Locate every blood parasite and identify its species.
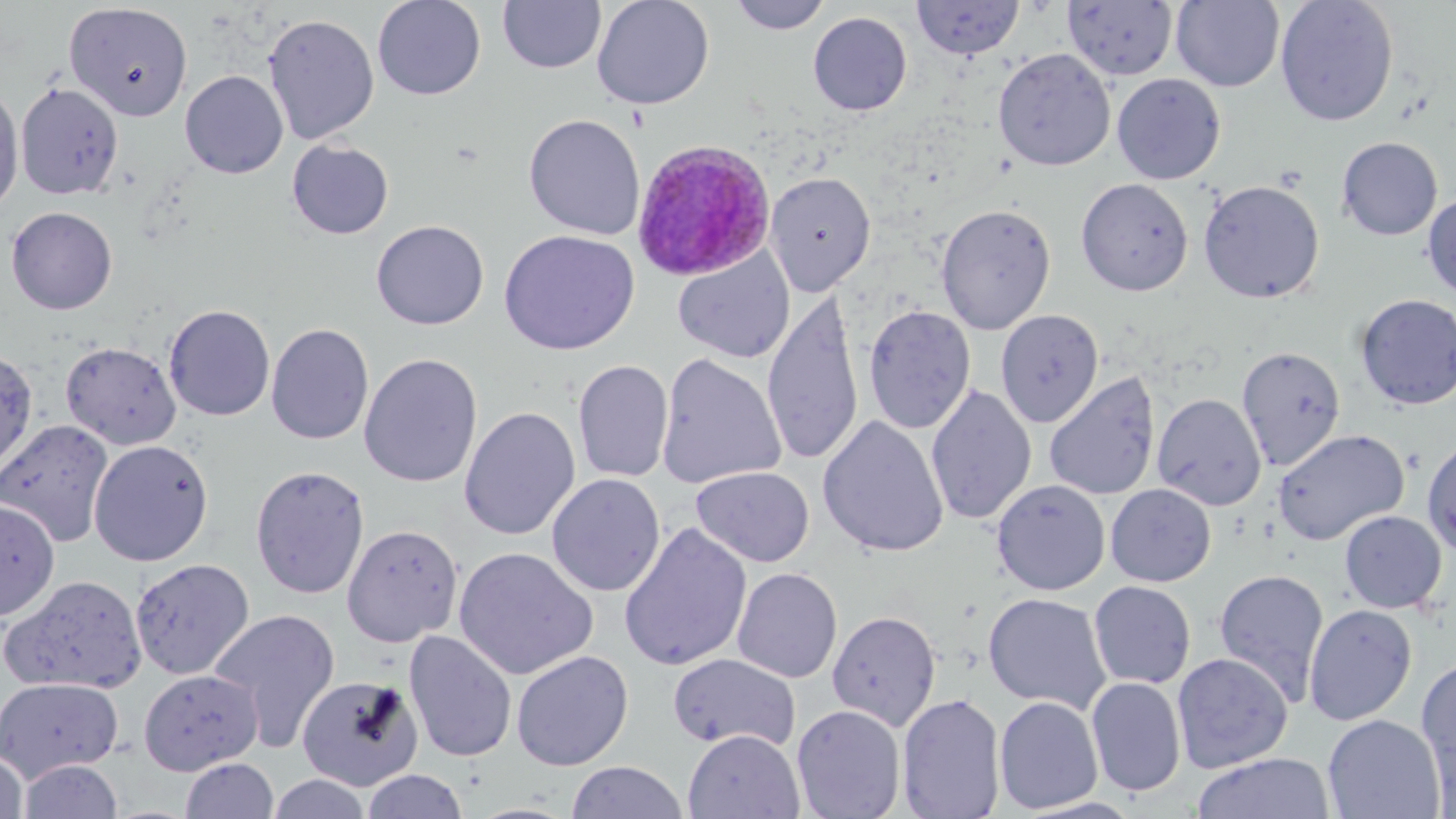
Approximate bounding boxes as (x1,y1)-(x2,y2) corner pairs in pixels.
Plasmodium ovale-infected red blood cells: (631,138)-(775,280).
No Plasmodium falciparum, Plasmodium malariae, Plasmodium vivax, Babesia divergens, or Trypanosoma brucei observed.

Uninfected red blood cell locations: (372,0)-(487,100), (592,0)-(715,110), (728,0)-(832,34), (912,0)-(1024,60), (1275,0)-(1399,126), (498,1)-(606,75), (1062,1)-(1178,81), (1171,1)-(1285,91), (64,3)-(193,121), (807,11)-(912,116), (263,14)-(380,144), (992,47)-(1116,171), (180,70)-(288,179), (1111,73)-(1226,185), (15,82)-(124,200), (0,84)-(24,217), (524,114)-(645,240), (1336,136)-(1443,240), (287,139)-(394,239), (765,172)-(876,296), (1076,178)-(1194,296), (1198,179)-(1325,304), (1422,192)-(1456,301), (936,203)-(1057,334), (5,206)-(117,314), (371,220)-(489,329), (499,230)-(640,355), (673,248)-(795,363), (1354,294)-(1456,410), (761,297)-(864,464), (163,304)-(276,421), (863,304)-(976,434), (864,308)-(1104,429), (995,309)-(1103,428), (266,323)-(374,445), (60,341)-(182,450), (1236,346)-(1346,471), (0,347)-(39,475), (358,352)-(483,488), (656,353)-(786,490), (572,359)-(674,482), (1044,371)-(1161,500), (925,384)-(1037,525), (1151,393)-(1266,510), (459,407)-(580,540), (818,415)-(949,558), (0,418)-(115,546), (1273,429)-(1409,546), (1421,435)-(1456,559), (88,439)-(214,566), (249,465)-(371,600), (691,466)-(814,567), (546,473)-(665,597), (992,479)-(1111,595), (1105,483)-(1217,587), (0,500)-(60,621), (1338,510)-(1447,614), (618,522)-(753,673), (341,523)-(464,647), (454,546)-(598,680), (129,558)-(255,680), (732,567)-(843,683), (1213,568)-(1330,706), (2,574)-(148,695), (1088,581)-(1196,690), (983,592)-(1111,714), (1303,604)-(1418,726), (207,608)-(340,752), (827,610)-(941,731), (404,630)-(518,762), (511,650)-(634,771), (1171,652)-(1293,773), (668,653)-(801,752), (1416,656)-(1456,791), (138,669)-(263,775), (297,674)-(423,790), (0,676)-(124,782), (1086,677)-(1187,797), (897,693)-(1007,818), (994,696)-(1104,814), (792,704)-(906,819), (1323,714)-(1446,819), (682,729)-(804,818), (0,751)-(29,819), (1190,753)-(1337,819), (179,757)-(279,819), (17,759)-(125,819), (565,761)-(688,818), (361,770)-(468,819), (267,773)-(373,818). Slide-level diagnosis: Plasmodium ovale. Single field of view. Thin blood film. Image is 1456×819 pixels. May-Grünwald-Giemsa-stained preparation. Light microscopy. Captured at 1000x magnification.